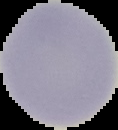
result = no malaria parasites detected
preparation = thin blood smear
image type = segmented cell region on a black background
image size = 118×130 pixels